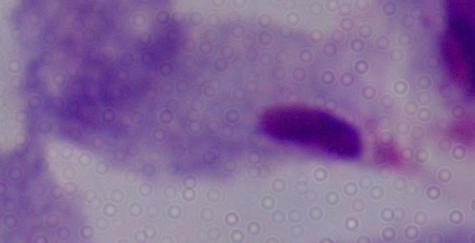
identification: trichomonad
magnification: 1000x
modality: photomicrograph